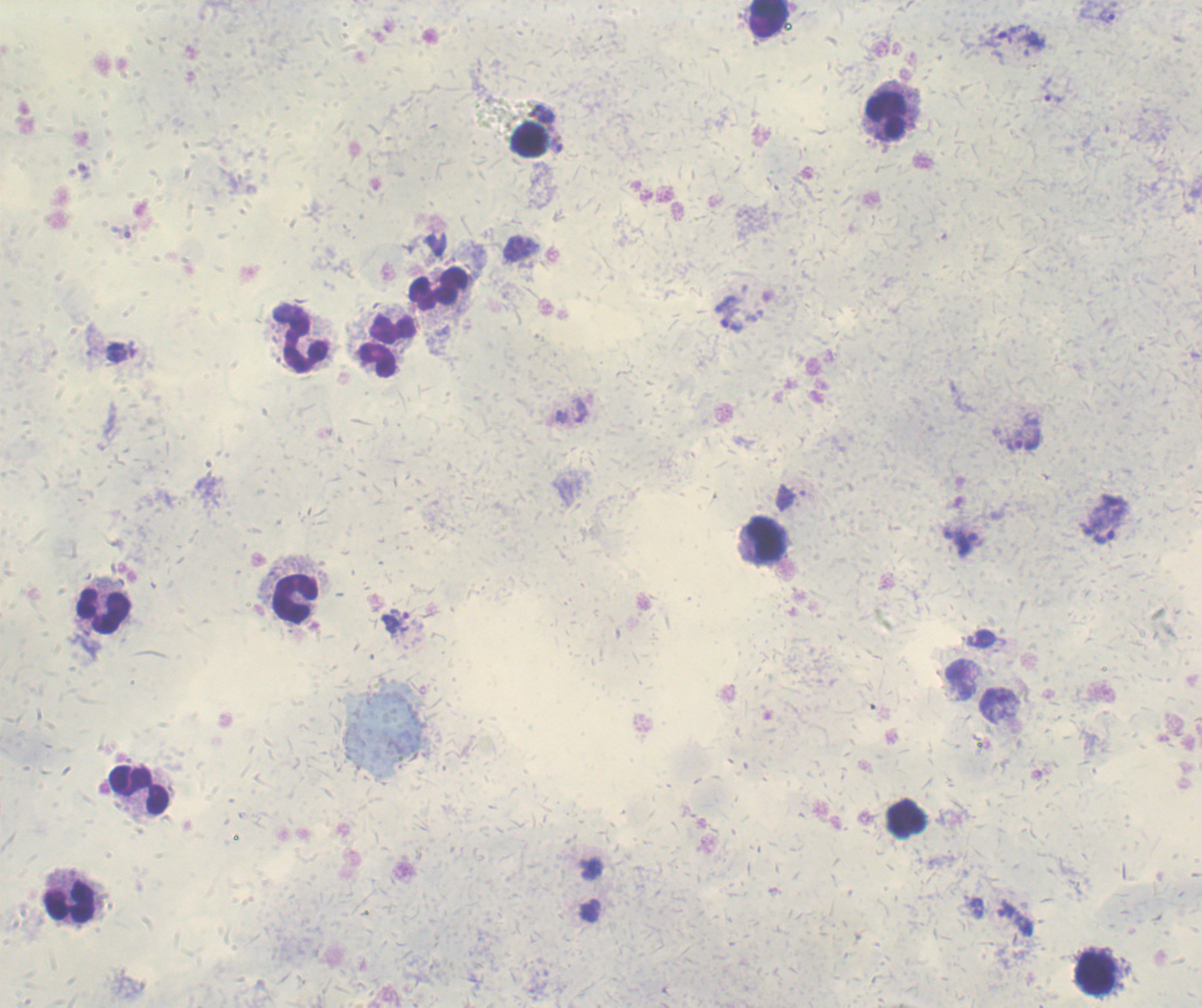
Approximate centers as [x, y] in pixels. Trophozoite locations: [1107, 16], [1032, 43], [1052, 94], [733, 325], [561, 417], [1023, 435], [1104, 520], [963, 542], [395, 622], [1000, 703]. Leukocyte locations: [768, 20], [885, 113], [529, 140], [439, 288], [390, 329], [301, 336], [376, 360], [763, 540], [293, 598], [104, 609], [139, 788], [905, 818], [69, 899], [1094, 972]. Image is 1202×1008 pixels. Thick smear of blood. Previously used in a real diagnosis. Result: malaria parasites identified. Background quality: unsatisfactory. Captured at 100x magnification. Coloration quality: good. One field from this slide. Romanowsky-stained preparation.